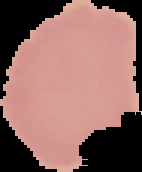
image size = 142×172 pixels
preparation = thin blood smear
image type = segmented cell region with the area outside set to black
result = no malaria parasites detected